Locate and identify every blood parasite.
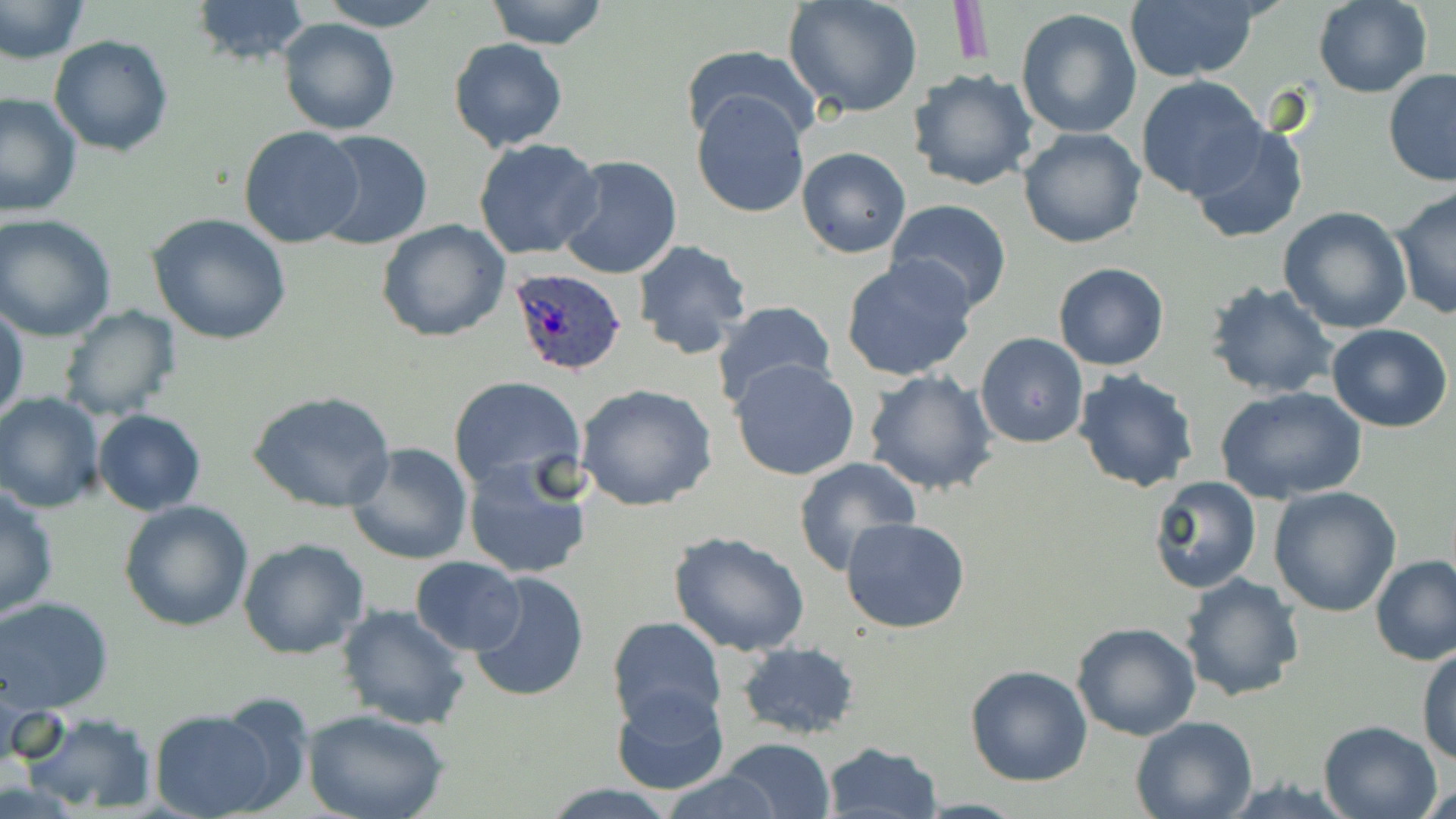

Approximate bounding boxes as [x1, y1, x2, y2] in pixels.
Plasmodium ovale-infected red blood cells: [507, 265, 629, 380].
No Plasmodium falciparum, Plasmodium malariae, Plasmodium vivax, Babesia divergens, or Trypanosoma brucei observed.

slide_level_diagnosis: Plasmodium ovale
preparation: thin blood smear
magnification: 1000x
image_size: 1456×819 pixels
uninfected_red_blood_cell_locations: 'approximate bounding boxes as [x1, y1, x2, y2] in pixels: [0, 0, 89, 66], [188, 0, 311, 68], [317, 0, 446, 31], [484, 0, 610, 48], [783, 0, 924, 120], [1124, 0, 1261, 82], [1313, 0, 1432, 98], [1015, 6, 1144, 140], [278, 18, 399, 135], [48, 34, 174, 157], [447, 38, 569, 153], [678, 47, 824, 149], [907, 68, 1038, 192], [1383, 69, 1456, 187], [1136, 76, 1267, 200], [0, 91, 83, 221], [691, 91, 810, 219], [1186, 121, 1310, 244], [238, 125, 367, 247], [1018, 127, 1147, 248], [311, 130, 434, 250], [473, 138, 603, 260], [796, 146, 912, 258], [554, 155, 684, 281], [1390, 188, 1455, 320], [885, 199, 1013, 315], [1278, 207, 1413, 334], [146, 213, 292, 344], [1, 214, 117, 340], [376, 219, 511, 341], [630, 238, 754, 361], [840, 257, 979, 383], [1053, 262, 1169, 371], [1204, 282, 1339, 401], [0, 301, 29, 426], [710, 301, 838, 416], [57, 306, 182, 422], [1328, 324, 1453, 433], [974, 332, 1088, 448], [729, 359, 862, 481], [862, 370, 1000, 496], [1073, 370, 1200, 494], [447, 374, 586, 494], [574, 383, 719, 513], [1214, 385, 1367, 505], [248, 390, 398, 515], [0, 393, 107, 512], [93, 408, 205, 514], [346, 443, 474, 566], [463, 456, 588, 580], [793, 456, 922, 575], [1147, 475, 1262, 595], [0, 485, 59, 620], [1268, 486, 1401, 617], [120, 500, 253, 632], [840, 518, 971, 635], [667, 531, 813, 659], [237, 537, 370, 659], [1370, 555, 1456, 666], [410, 557, 526, 654], [468, 570, 592, 701], [1183, 573, 1306, 703], [1, 598, 118, 715], [336, 604, 470, 732], [606, 615, 726, 731], [1072, 622, 1201, 740], [736, 641, 860, 741], [1417, 644, 1456, 766], [965, 665, 1093, 786], [611, 684, 730, 793], [148, 707, 285, 819], [17, 709, 160, 813], [306, 710, 448, 819], [1130, 715, 1258, 819], [1317, 719, 1443, 819], [719, 737, 835, 819], [820, 741, 943, 819], [656, 772, 783, 819], [538, 785, 678, 818]'
field_of_view: single
stain: May-Grünwald-Giemsa
modality: optical microscopy